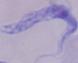

Summary:
  - Magnification: 1000x
  - Modality: micrograph
  - Identification: trypanosome